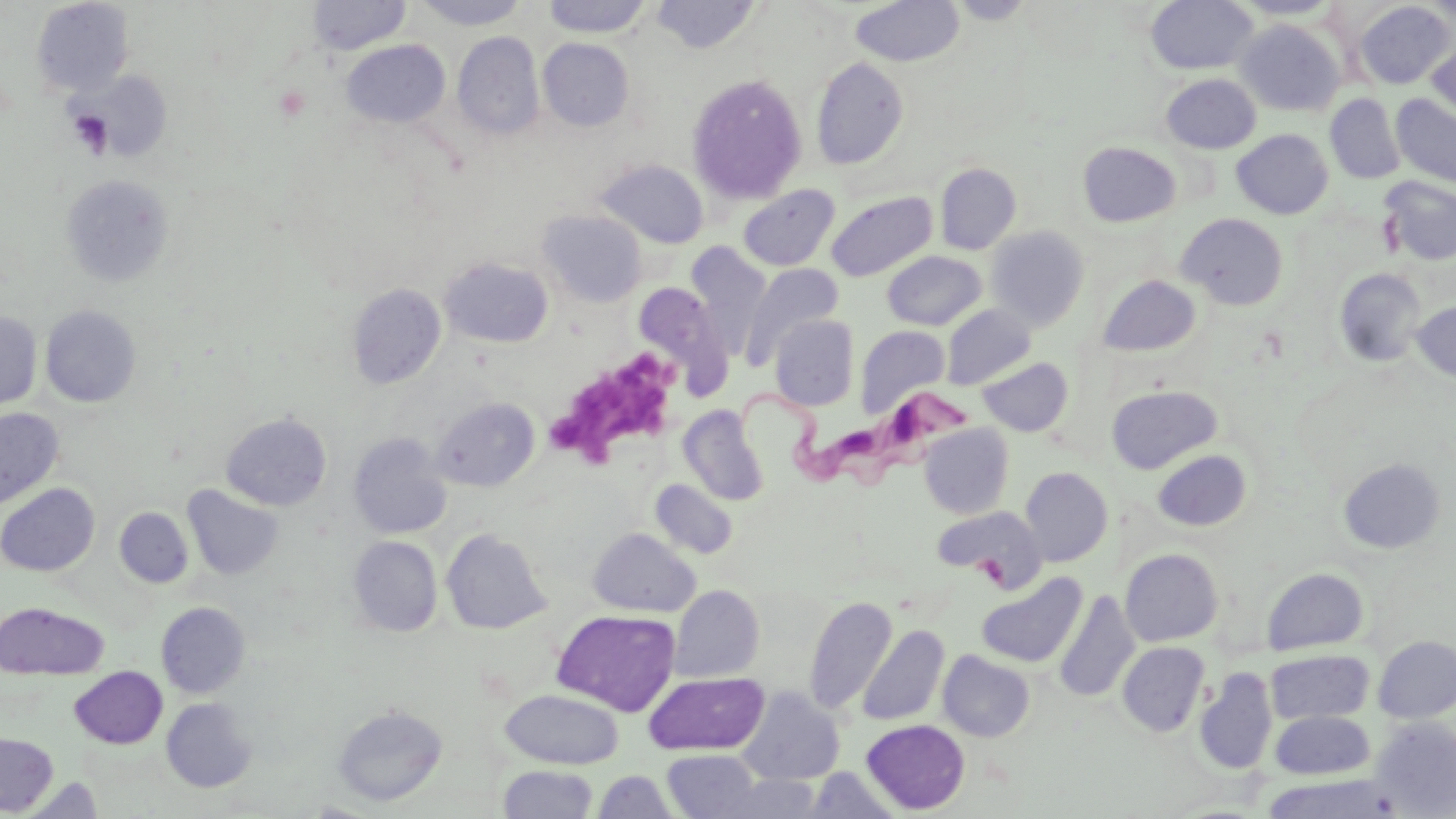
Summary:
  - Coordinate format: approximate bounding boxes as (x1, y1, x2, y2) in pixels
  - Trypanosoma brucei locations: (733, 379, 975, 490)
  - Uninfected red blood cell locations: (307, 0, 410, 55), (412, 0, 531, 30), (542, 0, 652, 37), (651, 0, 763, 55), (850, 0, 964, 67), (948, 0, 1038, 24), (1146, 0, 1258, 75), (1231, 0, 1342, 20), (31, 1, 134, 97), (1354, 1, 1454, 89), (1424, 1, 1456, 26), (1235, 19, 1344, 116), (452, 31, 545, 140), (1425, 33, 1456, 124), (538, 38, 635, 132), (341, 39, 451, 128), (811, 57, 909, 170), (1161, 73, 1262, 154), (687, 74, 807, 205), (1325, 94, 1405, 184), (1391, 94, 1456, 189), (1231, 129, 1333, 220), (1077, 142, 1181, 227), (595, 159, 709, 248), (935, 162, 1021, 255), (60, 174, 174, 288), (1379, 176, 1456, 265), (738, 185, 840, 271), (826, 191, 938, 281), (537, 209, 647, 307), (1177, 212, 1288, 311), (985, 226, 1089, 331), (685, 242, 772, 354), (882, 250, 986, 330), (440, 256, 553, 347), (740, 262, 843, 366), (1332, 268, 1427, 367), (1096, 275, 1201, 356), (634, 282, 731, 385), (346, 284, 446, 388), (1411, 299, 1456, 383), (941, 304, 1036, 390), (39, 305, 141, 407), (0, 311, 42, 413), (770, 314, 860, 411), (855, 325, 950, 419), (977, 357, 1074, 436), (1106, 384, 1222, 474), (431, 396, 540, 492), (677, 405, 769, 505), (0, 408, 63, 509), (221, 412, 332, 511), (919, 423, 1014, 518), (347, 433, 452, 539), (1152, 449, 1252, 531), (1338, 457, 1446, 554), (1020, 466, 1113, 566), (651, 479, 739, 559), (0, 483, 100, 576), (183, 485, 284, 581), (932, 506, 1047, 586), (115, 507, 193, 588), (440, 528, 551, 634), (588, 528, 700, 617), (348, 536, 442, 637), (1120, 549, 1223, 646), (1261, 567, 1368, 655), (976, 572, 1087, 668), (670, 585, 764, 682), (1054, 591, 1140, 703), (804, 595, 897, 715), (0, 602, 107, 679), (157, 602, 251, 698), (552, 609, 681, 716), (857, 625, 950, 726), (1373, 635, 1456, 723), (1117, 641, 1210, 737), (1266, 649, 1374, 725), (938, 650, 1035, 742), (69, 666, 167, 748), (1194, 668, 1276, 774), (644, 673, 768, 755), (737, 687, 845, 785), (500, 689, 624, 769), (162, 698, 257, 792), (332, 704, 447, 806), (1271, 710, 1374, 779), (1369, 718, 1456, 815), (862, 719, 970, 814), (0, 731, 58, 815), (662, 750, 765, 819), (498, 764, 599, 818), (804, 768, 900, 818), (592, 770, 680, 818), (1259, 773, 1402, 819), (24, 774, 105, 818), (717, 774, 824, 818)
  - Platelet locations: (66, 109, 114, 158), (549, 347, 683, 468)
  - Slide-level diagnosis: Trypanosoma brucei
  - Preparation: thin blood film
  - Magnification: 1000x
  - Field of view: one of a larger specimen
  - Modality: optical microscopy
  - Stain: May-Grünwald-Giemsa
  - Image size: 1456×819 pixels